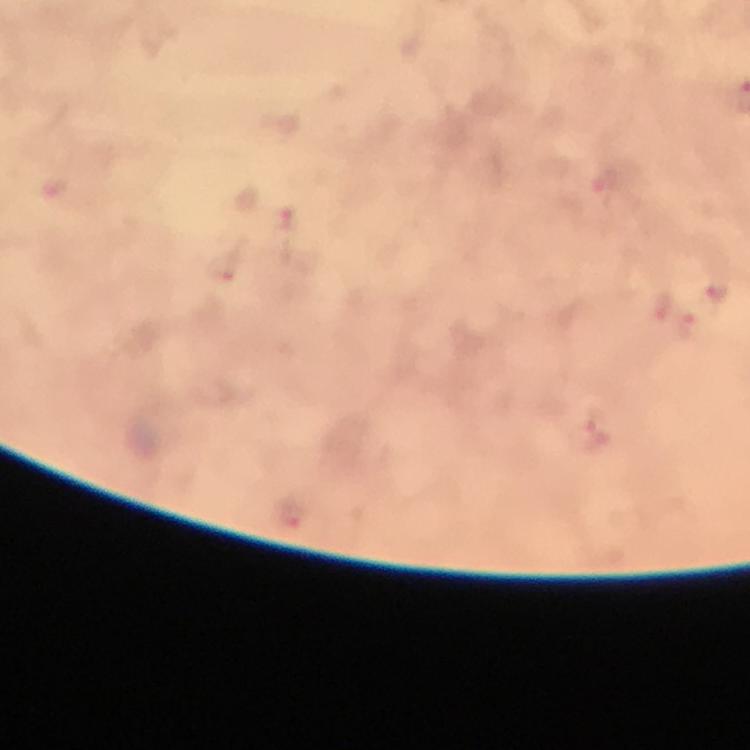
Approximate centers as (x, y) in pixels.
Summary:
  - Malaria parasite locations: (287, 220), (717, 293), (595, 435)
  - Cropped from: a single field of view
  - Stain: Giemsa
  - Context: from a malaria diagnostic workup
  - Magnification: 100x
  - Preparation: thick blood smear
  - Immersion oil: used
  - Capture: smartphone camera through the microscope
  - Image size: 750×750 pixels